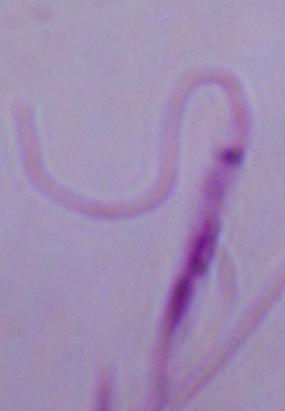

Summary:
  - Modality: micrograph
  - Magnification: 1000x
  - Identification: Leishmania